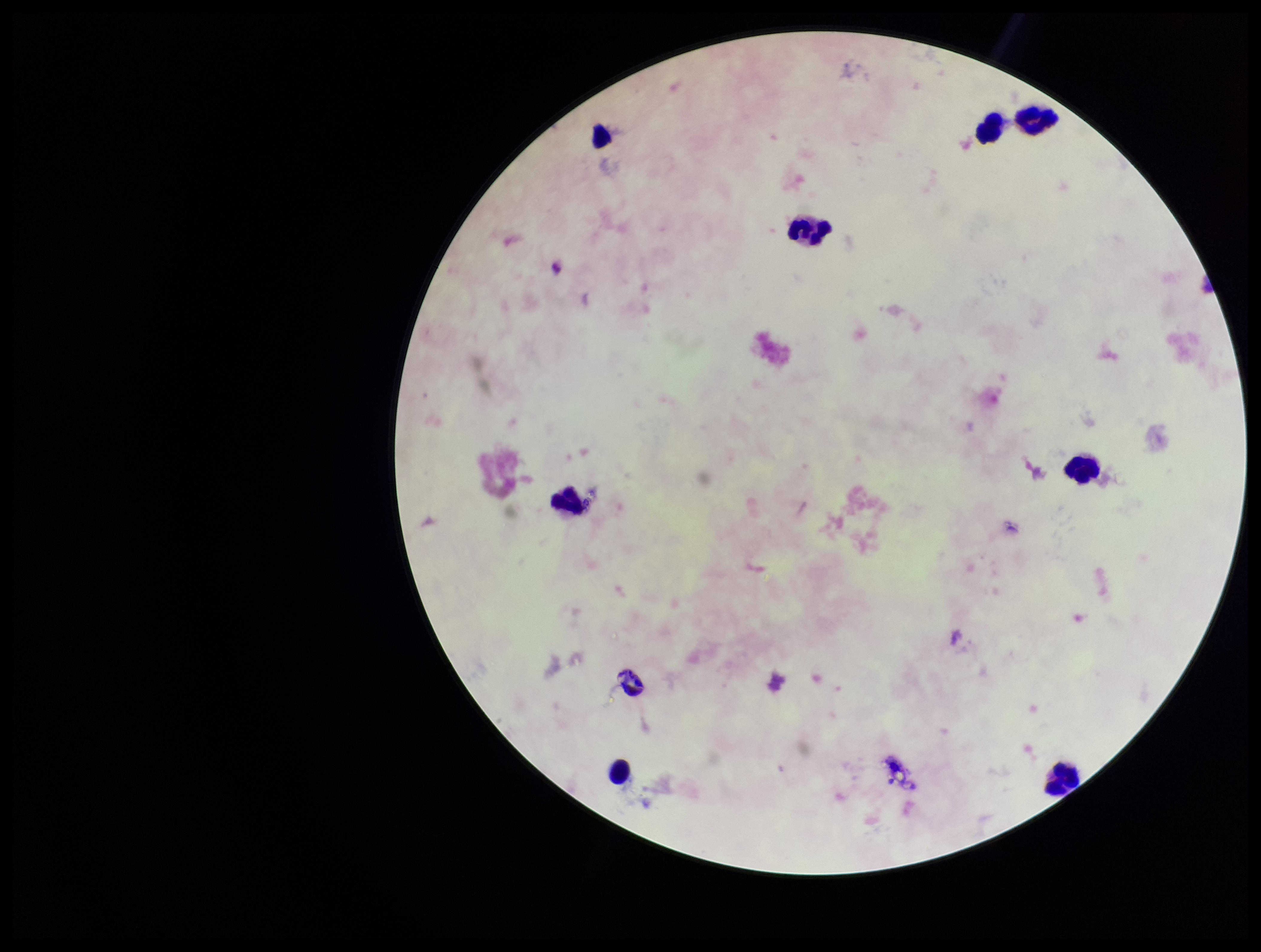 Plasmodium parasites: none seen. Giemsa stain. Preparation: thick. Species reported for this patient: Plasmodium falciparum. Patient malaria status: positive. Parasite count: 0. Single field of view. Image is 1261×952 pixels. Photographed through the microscope eyepiece with a smartphone camera. Leukocyte count: 9.